Outline each Plasmodium malariae-infected red blood cell.
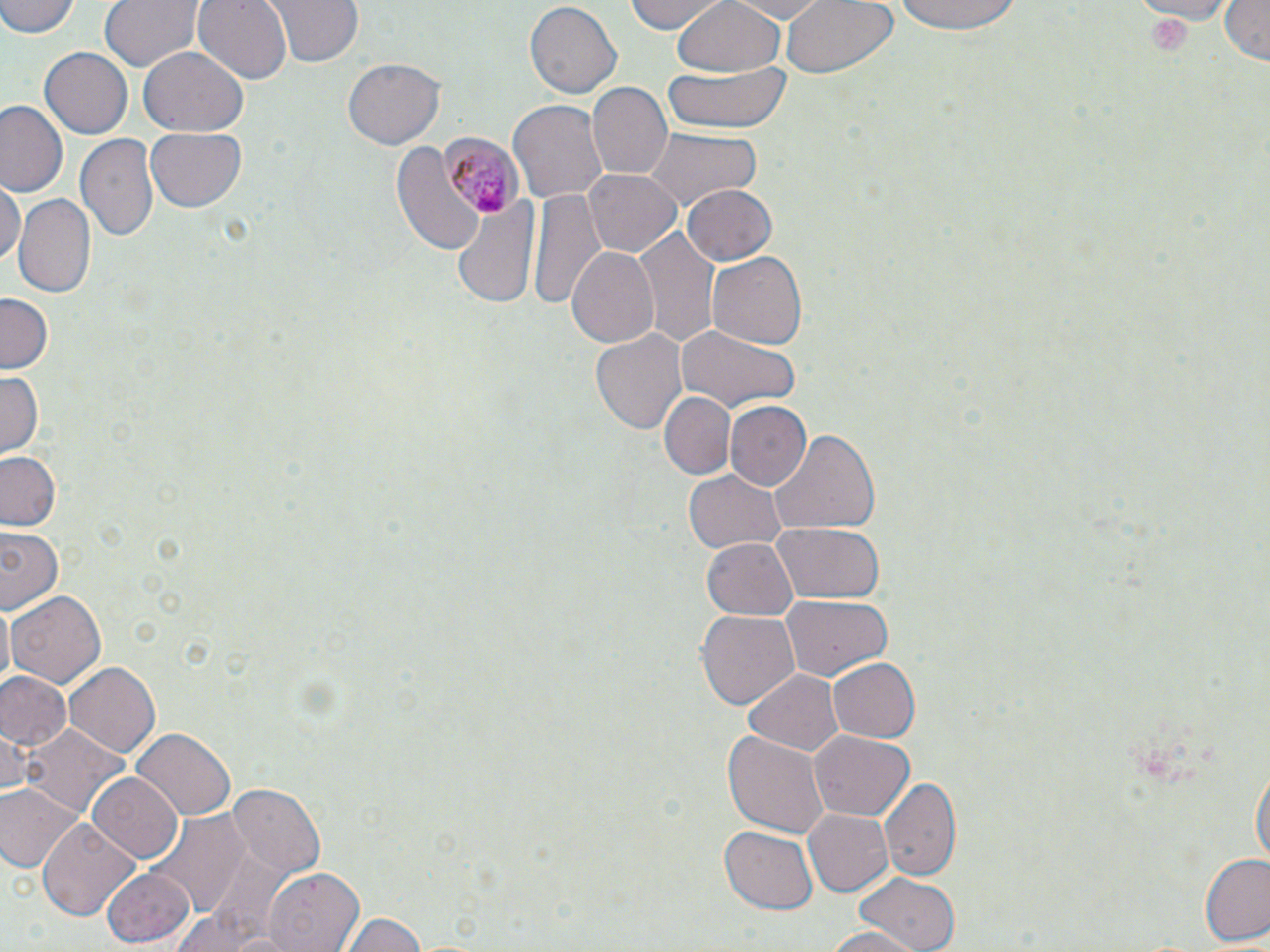
Approximate bounding boxes as (x1, y1, x2, y2) in pixels.
Plasmodium malariae-infected red blood cells: (440, 134, 518, 223).

Uninfected red blood cell locations: (0, 0, 81, 40), (99, 0, 202, 74), (193, 0, 291, 85), (259, 0, 366, 69), (623, 0, 729, 35), (669, 0, 789, 78), (720, 0, 836, 22), (777, 0, 896, 80), (892, 0, 1022, 38), (1124, 0, 1241, 22), (1218, 0, 1268, 65), (524, 4, 623, 100), (39, 44, 133, 137), (138, 46, 248, 137), (342, 59, 444, 149), (663, 62, 792, 135), (584, 84, 672, 182), (511, 99, 608, 206), (0, 100, 68, 200), (144, 127, 247, 212), (642, 129, 761, 208), (75, 133, 160, 244), (390, 139, 487, 258), (581, 168, 683, 258), (0, 181, 23, 268), (681, 184, 778, 268), (526, 187, 606, 314), (13, 195, 97, 301), (454, 197, 538, 307), (636, 224, 720, 347), (565, 246, 659, 350), (708, 251, 808, 351), (0, 291, 53, 370), (673, 323, 804, 413), (589, 324, 689, 438), (0, 372, 43, 455), (659, 390, 735, 480), (723, 400, 811, 491), (768, 430, 882, 536), (0, 450, 63, 530), (683, 470, 787, 554), (771, 521, 885, 603), (2, 527, 64, 614), (701, 537, 798, 622), (7, 589, 106, 688), (780, 592, 893, 679), (697, 609, 799, 711), (827, 659, 920, 742), (65, 662, 160, 758), (744, 667, 845, 753), (0, 672, 72, 752), (0, 723, 32, 800), (23, 725, 125, 819), (724, 728, 828, 838), (131, 729, 235, 820), (809, 731, 914, 819), (1251, 760, 1268, 875), (87, 773, 183, 862), (878, 778, 962, 880), (232, 785, 323, 878), (0, 786, 81, 876), (803, 809, 894, 898), (148, 812, 250, 917), (37, 818, 140, 921), (719, 826, 818, 914), (1198, 852, 1270, 947), (261, 865, 363, 951), (103, 869, 195, 947), (851, 870, 964, 951), (172, 911, 288, 949), (340, 912, 428, 952), (817, 926, 926, 952). Slide-level diagnosis: Plasmodium malariae. Captured at 1000x magnification. Optical microscopy. Image is 1270×952 pixels. Single field of view. Thin blood film. May-Grünwald-Giemsa stain.